Classify this cell by malaria status.
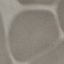

Uninfected.

Summary:
  - Image type: automatically extracted cell patch, resized to 64 × 64 pixels
  - Stain: Giemsa
  - Capture: smartphone through the microscope eyepiece
  - Preparation: thin blood film